Assess this cell for malaria.
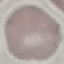
Uninfected.

Thin smear of blood. Giemsa-stained preparation. Cell patch, automatically extracted from a larger field of view and resized to 64 × 64 pixels. Acquired by smartphone through the microscope eyepiece.